Locate every Plasmodium parasite.
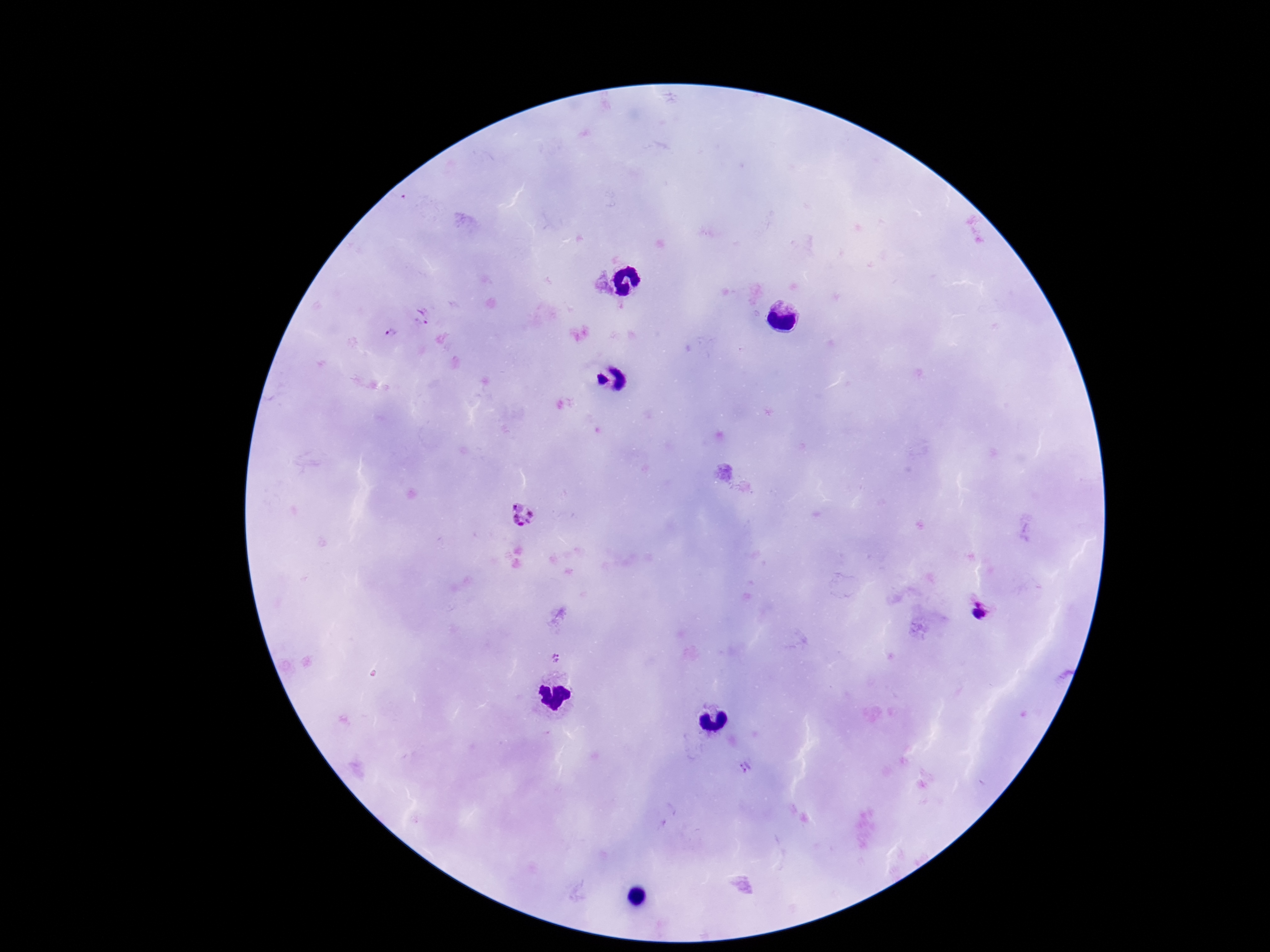

Approximate centers as (x, y) in pixels.
Plasmodium parasites: (522, 517), (980, 611), (555, 658), (745, 767).

Summary:
  - Patient malaria status: infected
  - Stain: Giemsa
  - Magnification: 100x
  - Image size: 1270×952 pixels
  - Capture: smartphone camera through the microscope eyepiece
  - Preparation: thick blood smear
  - Field of view: one from this slide